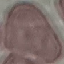

Malaria status: uninfected. Acquired by smartphone through the microscope eyepiece. Cell patch, automatically extracted from a larger field of view and resized to 64 × 64 pixels. Giemsa-stained preparation. Thin blood film.